Find each white blood cell.
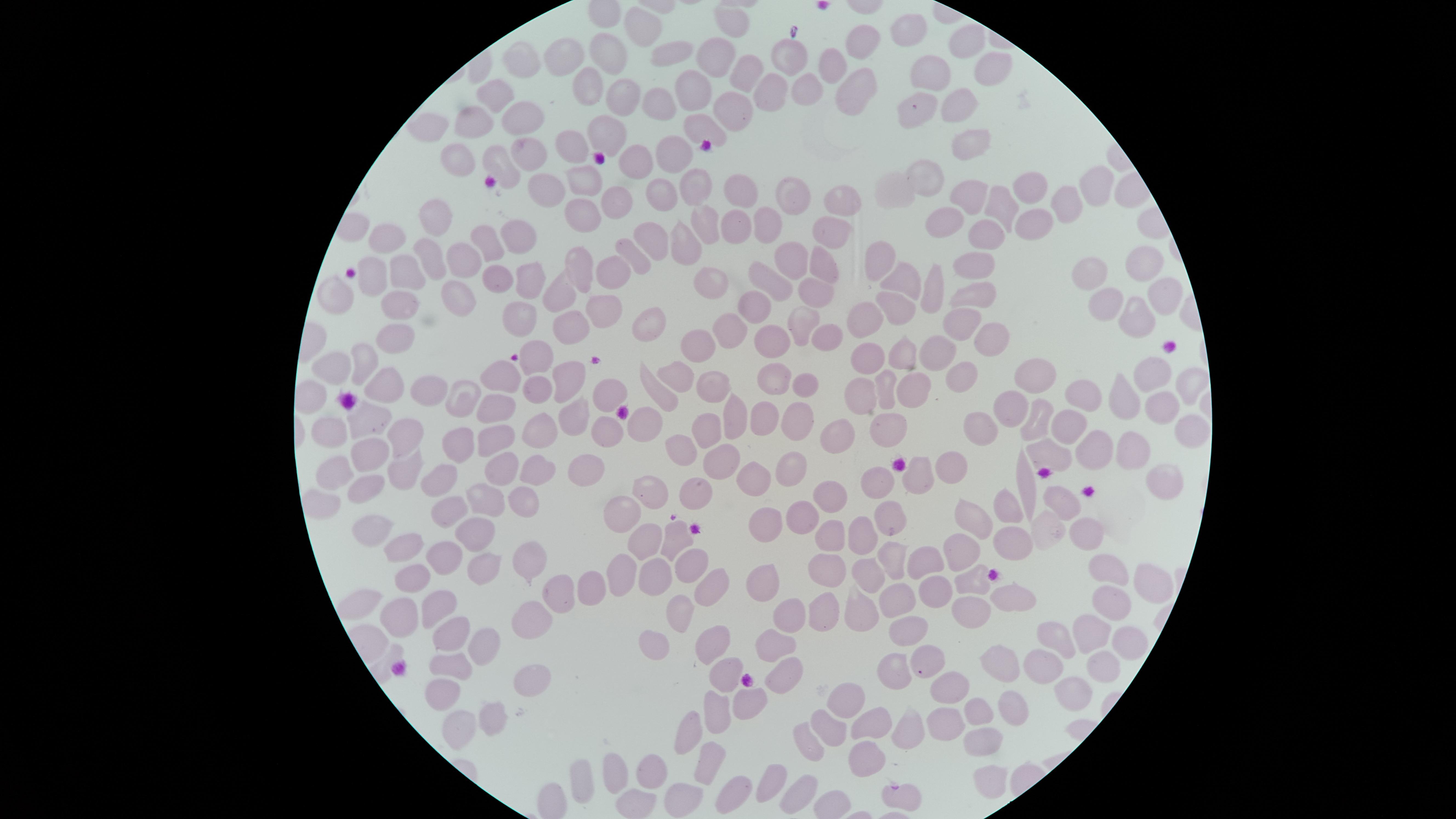

No white blood cells identified.

Approximate marker points as (x, y) in pixels.
Summary:
  - Uninfected red blood cells: (729, 20), (642, 27), (909, 29), (969, 36), (862, 39), (677, 42), (613, 51), (794, 55), (718, 56), (574, 58), (525, 62), (829, 64), (991, 64), (927, 66), (749, 67), (852, 83), (620, 85), (589, 86), (692, 88), (764, 88), (804, 88), (496, 91), (918, 101), (658, 102), (959, 106), (737, 110), (524, 116), (475, 121), (701, 122), (435, 124), (607, 133), (571, 144), (968, 144), (530, 149), (668, 149), (459, 154), (642, 159), (501, 165), (923, 175), (582, 176), (1098, 179), (692, 182), (743, 187), (893, 187), (1029, 188), (555, 193), (660, 195), (797, 195), (621, 196), (840, 196), (971, 201), (1073, 203), (1004, 205), (441, 209), (585, 214), (701, 217), (941, 217), (1033, 218), (765, 222), (733, 224), (833, 229), (987, 232), (525, 235), (388, 239), (651, 239), (682, 240), (491, 249), (635, 256), (1142, 258), (880, 259), (428, 260), (791, 260), (825, 261), (580, 264), (462, 265), (1091, 265), (977, 267), (407, 269), (613, 270), (373, 275), (492, 277), (900, 280), (934, 282), (529, 283), (770, 283), (706, 285), (559, 289), (338, 292), (1165, 292), (817, 295), (452, 296), (982, 297), (756, 305), (601, 306), (895, 306), (1105, 306), (401, 309), (1135, 313), (802, 316), (956, 316), (861, 317), (645, 318), (570, 321), (524, 322), (727, 325), (985, 332), (768, 334), (832, 334), (399, 336), (902, 345), (695, 346), (934, 347), (862, 350), (366, 355), (537, 355), (336, 366), (1151, 374), (571, 375), (681, 375), (772, 375), (504, 376), (1045, 377), (960, 379), (1183, 381), (534, 384), (714, 384), (801, 384), (386, 385), (886, 387), (912, 387), (425, 388), (659, 390), (1088, 392), (864, 393), (1118, 395), (610, 396), (458, 398), (1156, 399), (1013, 400), (503, 406), (572, 410), (799, 412), (370, 414), (764, 414), (727, 416), (1041, 417), (333, 422), (642, 422), (886, 422), (842, 426), (984, 428), (1072, 429), (405, 430), (1194, 430), (540, 432), (702, 432), (602, 434), (498, 435), (463, 440), (1126, 443), (680, 445), (1048, 447), (1094, 448), (719, 457), (362, 458), (585, 461), (950, 461), (499, 465), (407, 466), (532, 466), (334, 467), (788, 469), (919, 472), (1168, 476), (448, 479), (758, 479), (1027, 479), (888, 484), (368, 488), (649, 492), (698, 493), (1069, 496), (494, 497), (531, 501), (831, 501), (1009, 502), (624, 510), (453, 511), (806, 513), (978, 518), (886, 520), (1048, 522), (384, 525), (771, 525), (1098, 529), (680, 533), (470, 536), (857, 537), (831, 539), (647, 541), (1006, 542), (406, 545), (960, 553), (536, 556), (449, 557), (897, 557), (691, 559), (923, 562), (483, 564), (828, 565), (1115, 569), (865, 575), (419, 577), (971, 577), (657, 578), (592, 580), (763, 581), (1152, 581), (906, 590), (935, 590), (713, 592), (563, 596), (1004, 596), (360, 600), (441, 602), (858, 605), (1109, 607), (970, 608), (394, 612), (832, 612), (788, 613), (684, 619), (525, 625), (907, 629), (1088, 632), (462, 636), (1057, 636), (774, 639), (653, 640), (1125, 643), (486, 644), (714, 645), (931, 660), (1011, 666), (1101, 666), (454, 667), (781, 670), (894, 670), (727, 671), (1042, 671), (951, 683), (524, 686), (441, 689), (853, 693), (758, 695), (1072, 695), (1012, 699), (716, 713), (977, 713), (491, 718), (875, 726), (689, 727), (452, 729), (830, 729), (907, 730), (981, 736), (806, 741), (710, 753), (865, 760), (621, 773), (659, 773), (986, 777), (772, 779), (740, 789), (798, 789), (681, 792), (899, 792), (635, 804)
  - Stain: Giemsa
  - Preparation: thin blood smear
  - Visible region: circular
  - Presence: no malaria parasites identified
  - Field of view: single
  - Capture: smartphone photograph through the microscope eyepiece
  - Image size: 1456×819 pixels